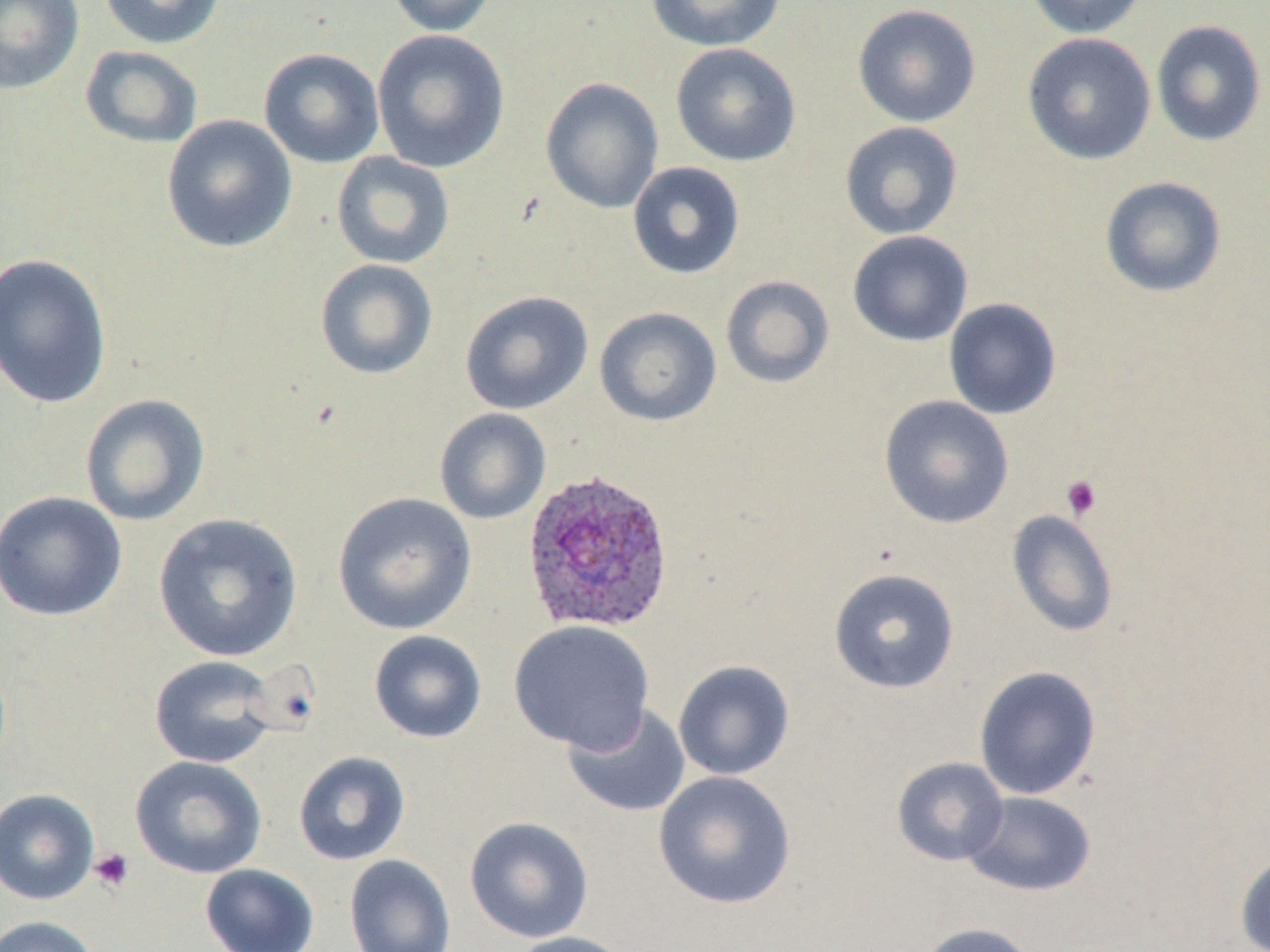

plasmodium_ovale_infected_red_blood_cell_locations: 'approximate bounding boxes as [x1, y1, x2, y2] in pixels: [520, 468, 676, 635]'
slide_level_diagnosis: Plasmodium ovale
preparation: thin blood smear
modality: light microscopy
uninfected_red_blood_cell_locations: 'approximate bounding boxes as [x1, y1, x2, y2] in pixels: [0, 0, 84, 95], [99, 0, 226, 50], [385, 0, 499, 37], [646, 0, 785, 51], [1023, 0, 1149, 39], [852, 4, 981, 127], [1151, 20, 1267, 147], [372, 29, 510, 173], [1022, 32, 1156, 165], [670, 43, 801, 167], [80, 45, 204, 149], [258, 48, 384, 169], [541, 77, 663, 214], [161, 114, 298, 254], [839, 122, 963, 240], [331, 151, 455, 269], [627, 161, 746, 280], [1099, 176, 1227, 298], [847, 231, 973, 347], [0, 252, 112, 408], [315, 258, 438, 380], [720, 275, 835, 389], [460, 290, 593, 414], [943, 298, 1062, 420], [594, 307, 722, 427], [79, 394, 211, 527], [879, 394, 1014, 529], [434, 408, 551, 525], [0, 490, 127, 622], [332, 492, 477, 635], [1007, 510, 1119, 637], [153, 512, 303, 662], [828, 568, 960, 694], [508, 619, 655, 753], [368, 630, 487, 744], [149, 655, 281, 768], [673, 660, 795, 780], [974, 665, 1101, 800], [562, 702, 690, 818], [293, 751, 411, 866], [129, 755, 267, 879], [891, 756, 1009, 866], [653, 770, 796, 909], [0, 788, 99, 905], [961, 790, 1097, 897], [464, 816, 594, 942], [1235, 850, 1270, 952], [344, 854, 456, 952], [200, 863, 320, 952], [0, 915, 102, 952], [917, 922, 1038, 952], [504, 931, 635, 952]'
stain: May-Grünwald-Giemsa
platelet_locations: 'approximate bounding boxes as [x1, y1, x2, y2] in pixels: [1060, 475, 1102, 520], [89, 848, 134, 892]'
magnification: 1000x
image_size: 1270×952 pixels
field_of_view: single